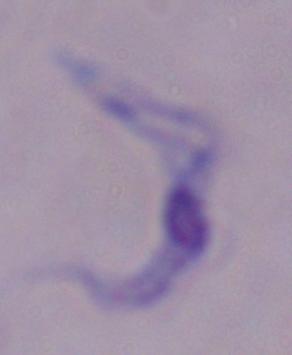

Summary:
  - Identification: trypanosome
  - Magnification: 1000x
  - Modality: photomicrograph